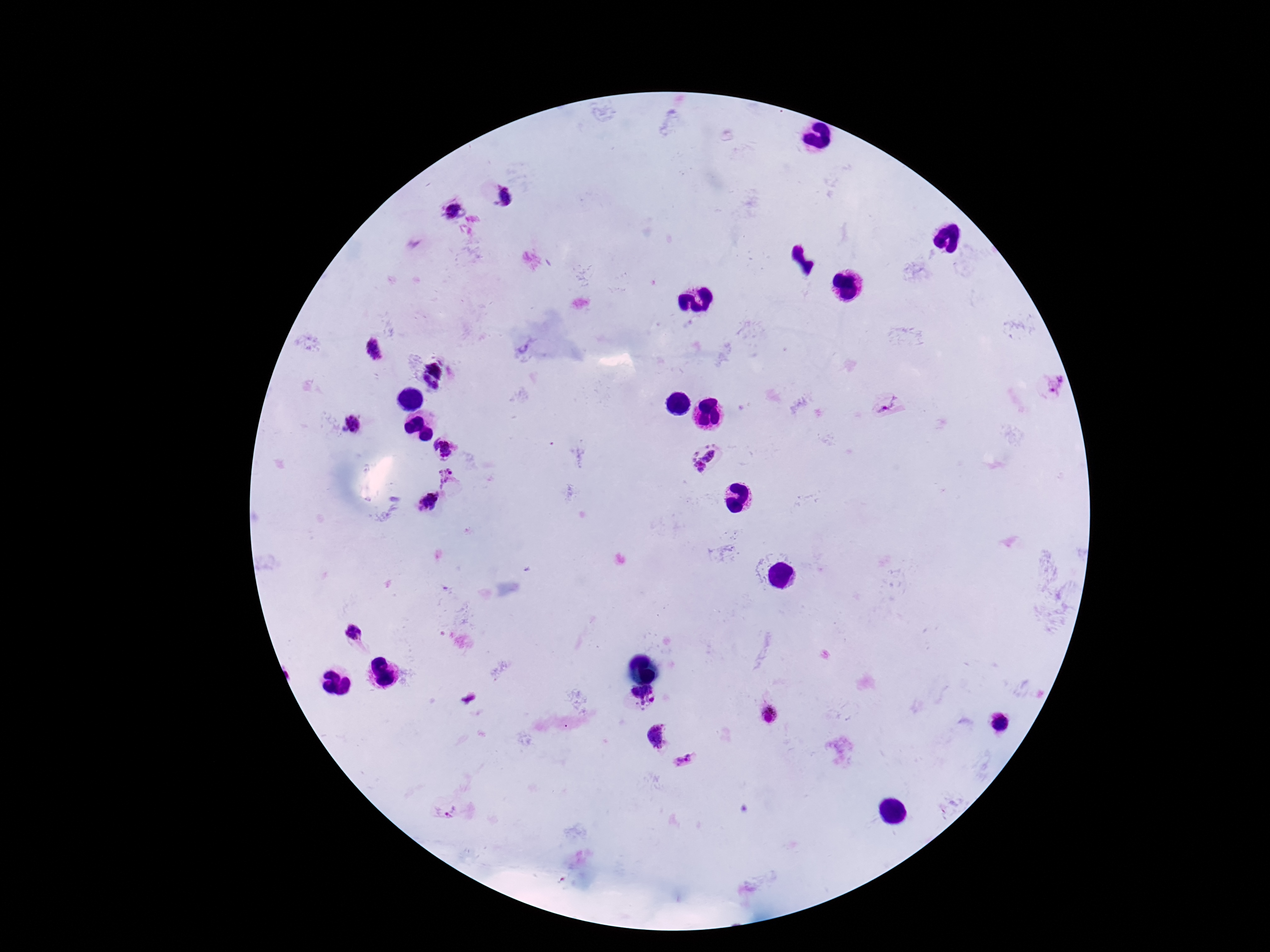 Approximate object centers, in pixels from the top-left corner. Plasmodium parasite locations: (x=506, y=196), (x=450, y=210), (x=374, y=349), (x=435, y=368), (x=427, y=380), (x=435, y=385), (x=1055, y=385), (x=888, y=406), (x=354, y=426), (x=444, y=447), (x=705, y=457), (x=444, y=478), (x=428, y=502), (x=354, y=632), (x=643, y=696), (x=768, y=713), (x=656, y=735), (x=683, y=761). Patient malaria status: infected. Giemsa stain. Single field of view. Thick blood smear. Photographed through the microscope eyepiece with a smartphone camera. Image is 1270×952 pixels. 100x magnification.